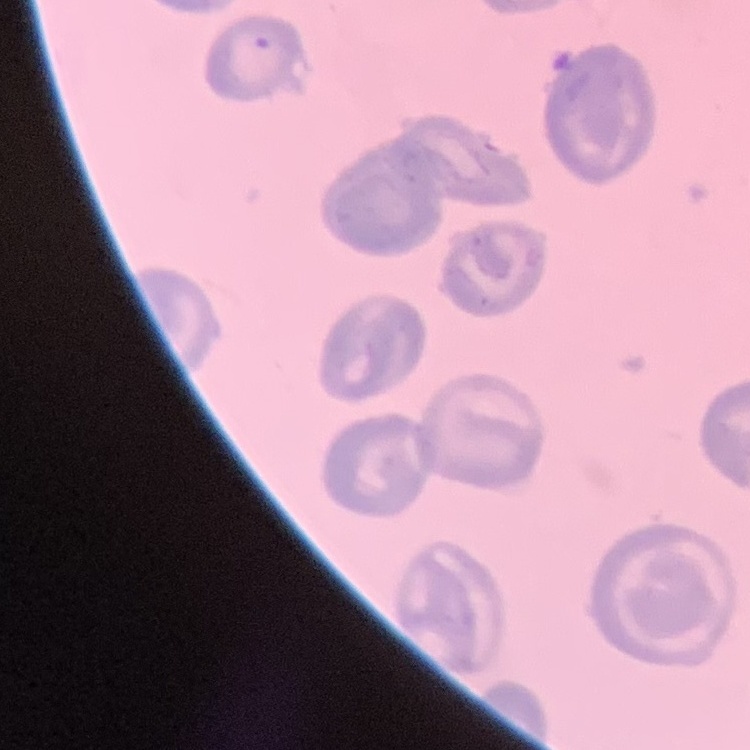

erythrocyte morphology = no rouleaux formation
image type = one tile cut from a larger photomicrograph
stain = Field's or Giemsa
preparation = thin blood smear